Identify the parasite.
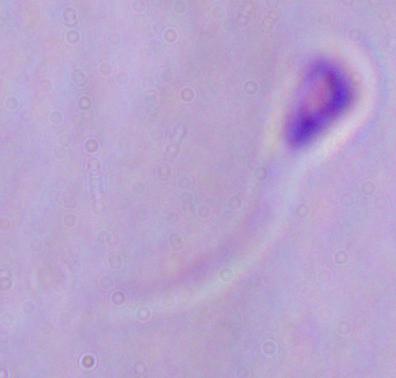

Leishmania.

Summary:
  - Magnification: 1000x
  - Modality: photomicrograph